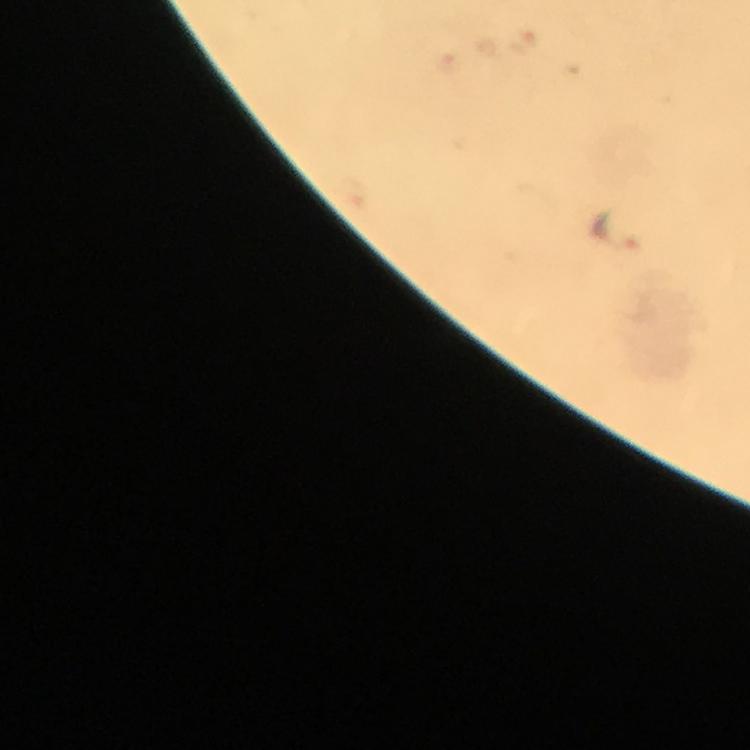
Approximate centers as [x, y] in pixels. Malaria parasite locations: [620, 232]. Image is 750×750 pixels. From a diagnostic examination for malaria. Immersion oil applied. Giemsa stain. 100x magnification. Smartphone photograph taken through a microscope. Thick smear. A crop from one field of view.